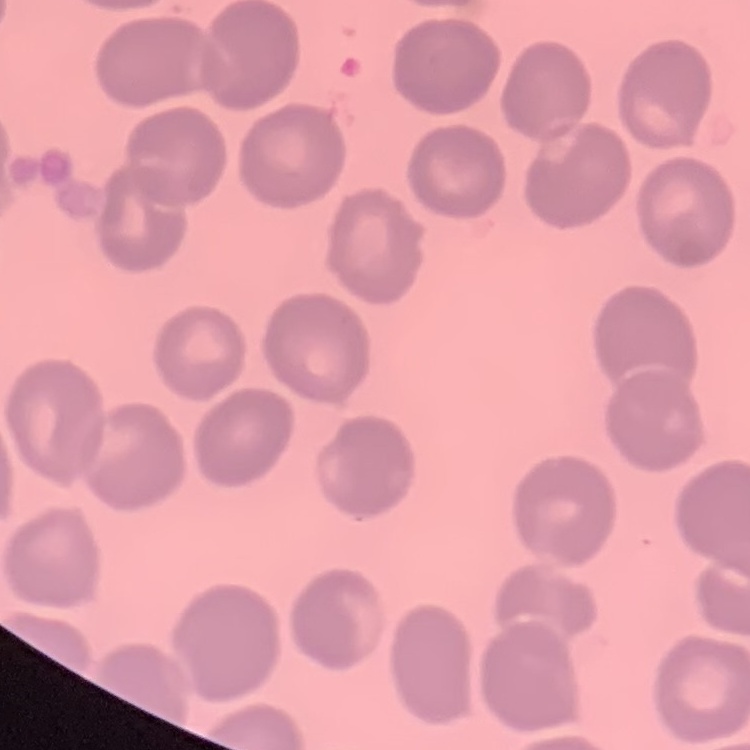

red blood cell morphology = no rouleaux formation
stain = Field's or Giemsa
preparation = thin blood smear
image type = square crop of a larger photomicrograph